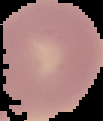

image size = 103×121 pixels
result = no malaria parasites seen
image type = cell region segmented out of the field of view; surrounding area masked to black
preparation = thin blood film